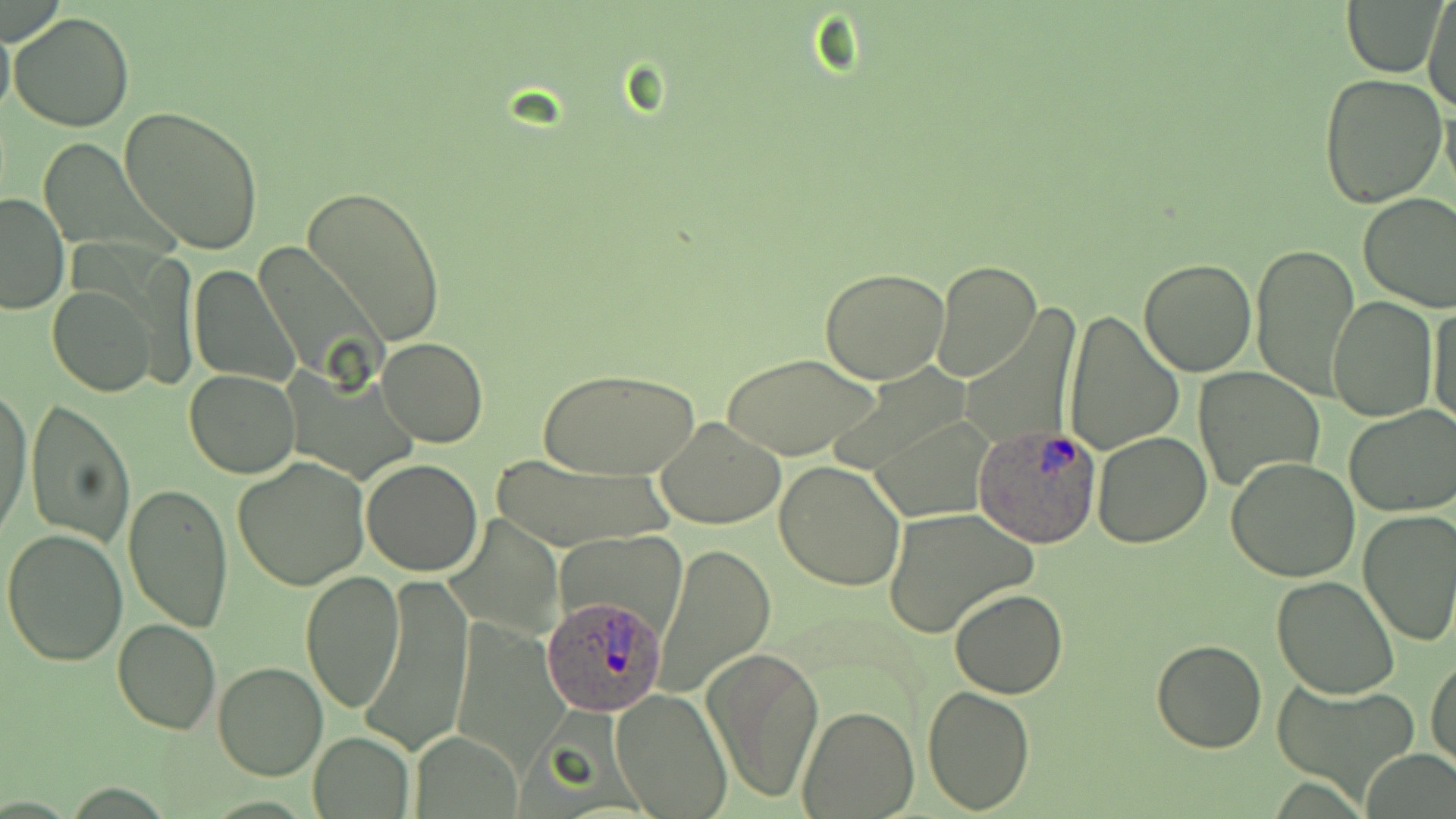 Approximate bounding boxes as (x1,y1)-(x2,y2) corner pairs in pixels. Plasmodium ovale-infected red blood cell locations: (976,426)-(1102,547), (542,595)-(666,715). Uninfected red blood cell locations: (1423,0)-(1456,113), (1343,1)-(1443,78), (8,12)-(134,131), (0,17)-(15,121), (1317,72)-(1448,210), (119,105)-(265,256), (302,185)-(446,347), (1358,192)-(1456,311), (1,193)-(70,313), (1249,243)-(1359,401), (1136,257)-(1256,377), (931,260)-(1041,383), (188,265)-(300,388), (820,266)-(950,383), (49,286)-(157,396), (1328,294)-(1438,423), (1429,297)-(1453,427), (1061,309)-(1185,458), (377,338)-(488,447), (723,353)-(881,460), (537,365)-(700,480), (1194,365)-(1326,492), (183,368)-(301,478), (822,369)-(974,477), (1,386)-(33,540), (26,400)-(134,547), (1344,404)-(1456,517), (871,413)-(995,520), (656,418)-(785,529), (1092,431)-(1213,549), (490,453)-(673,552), (231,456)-(373,592), (1225,457)-(1360,582), (361,459)-(483,576), (774,459)-(907,592), (122,483)-(234,632), (1356,507)-(1456,647), (883,508)-(1036,637), (445,513)-(566,638), (558,527)-(689,643), (3,528)-(129,667), (657,544)-(776,697), (301,569)-(404,713), (365,571)-(473,758), (1271,576)-(1399,698), (950,587)-(1067,698), (113,618)-(222,734), (1150,638)-(1269,753), (703,644)-(826,804), (1427,652)-(1455,773), (213,661)-(327,780), (1274,683)-(1423,798), (921,684)-(1035,814), (613,690)-(732,818), (798,705)-(918,817), (412,730)-(525,817), (307,732)-(415,817). Slide-level diagnosis: Plasmodium ovale. Captured at 1000x magnification. May-Grünwald-Giemsa-stained preparation. One field of a larger specimen. Light microscopy. Image is 1456×819 pixels. Thin blood film.